Identify the cell.
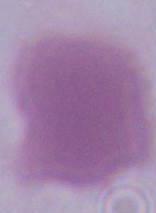
This is an erythrocyte.

Summary:
  - Modality: micrograph
  - Magnification: 1000x